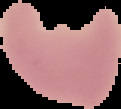
Result: malaria parasites identified. Cell region segmented out of the field of view; the surrounding area is masked to black. From a thin blood smear. Image is 121×109 pixels.